Name the cell type shown.
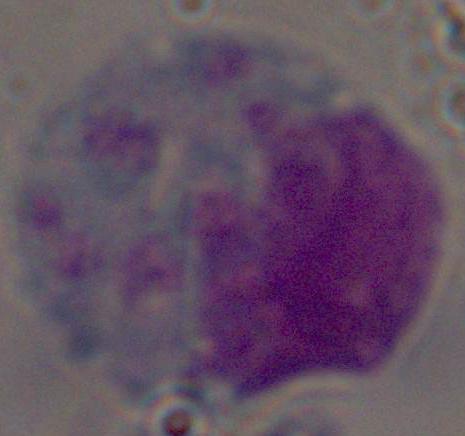
This is a leukocyte.

modality = micrograph
magnification = 1000x